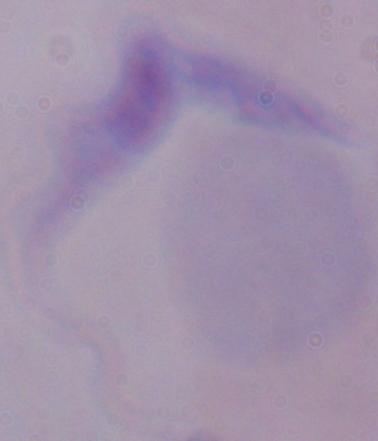 Micrograph. Captured at 1000x magnification. A trypanosome is seen.